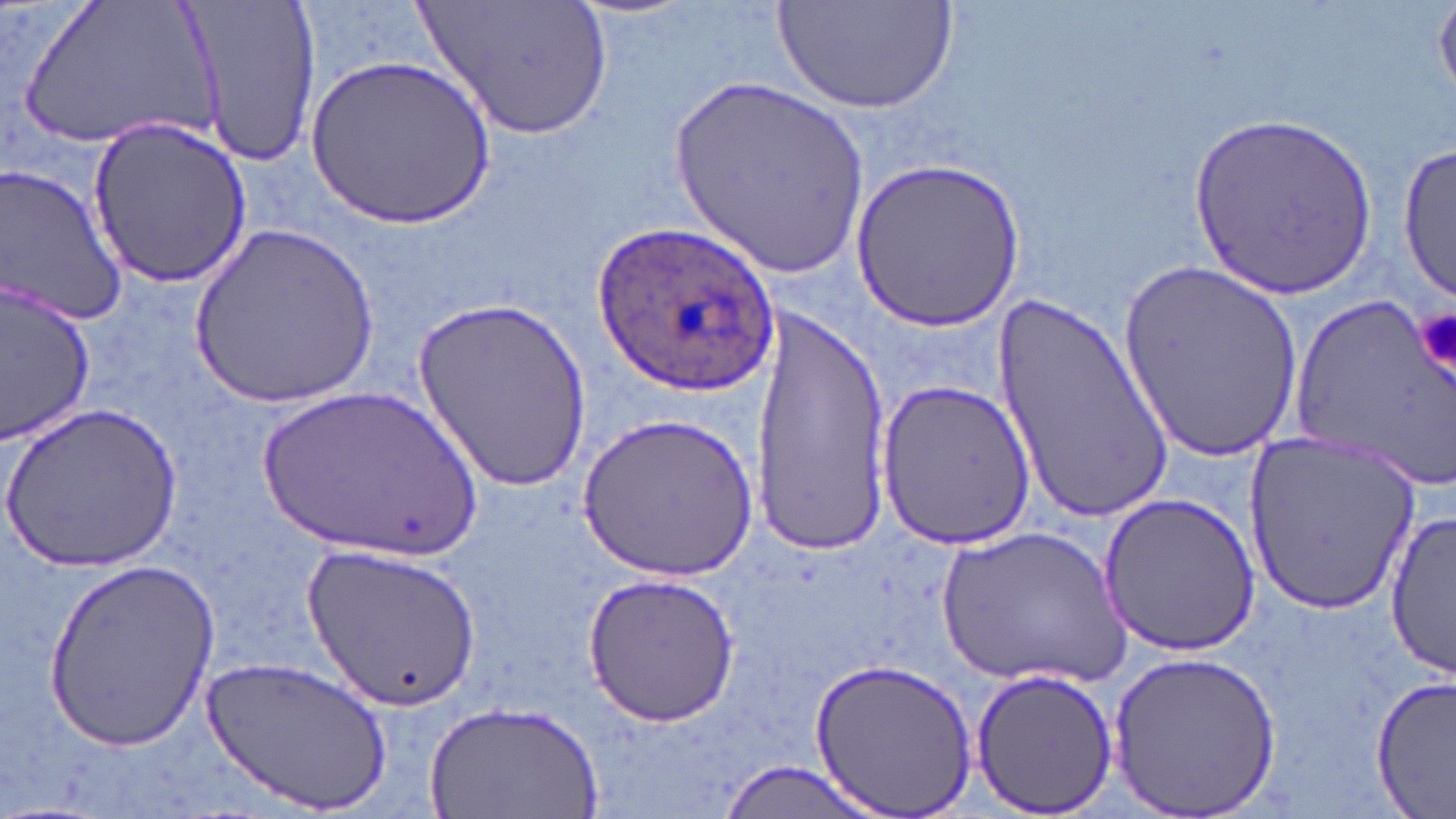
Plasmodium ovale-infected red blood cell locations = approximate bounding boxes as (x1, y1, x2, y2) in pixels: (591, 217, 772, 399)
slide-level diagnosis = Plasmodium ovale
magnification = 1000x
uninfected red blood cell locations = approximate bounding boxes as (x1, y1, x2, y2) in pixels: (21, 0, 222, 158), (181, 0, 322, 172), (417, 0, 614, 141), (772, 0, 962, 116), (1435, 3, 1456, 100), (308, 52, 494, 231), (672, 74, 871, 280), (1189, 109, 1376, 304), (85, 116, 256, 286), (1396, 140, 1453, 304), (848, 157, 1026, 333), (0, 164, 128, 330), (188, 222, 379, 410), (1119, 256, 1303, 459), (0, 282, 97, 443), (995, 290, 1174, 525), (1294, 290, 1455, 486), (412, 297, 591, 493), (752, 302, 892, 551), (876, 378, 1036, 549), (255, 382, 489, 567), (4, 399, 182, 571), (579, 414, 757, 581), (1244, 433, 1421, 615), (1098, 494, 1260, 657), (1386, 510, 1454, 678), (935, 525, 1132, 689), (306, 542, 481, 709), (44, 555, 222, 752), (582, 573, 740, 727), (1105, 649, 1285, 817), (202, 653, 391, 816), (809, 656, 977, 818), (972, 667, 1118, 816), (1373, 676, 1455, 817), (424, 701, 601, 819), (710, 761, 888, 819)
preparation = thin blood film
platelet locations = approximate bounding boxes as (x1, y1, x2, y2) in pixels: (1414, 305, 1455, 382)
modality = optical microscopy
field of view = one of a larger specimen
image size = 1456×819 pixels
stain = May-Grünwald-Giemsa